Name the parasite shown.
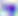
Toxoplasma gondii.

modality = photomicrograph
magnification = 400x